Classify this cell by malaria status.
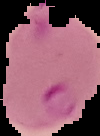

Parasitized.

Summary:
  - Image type: segmented cell region on a black background
  - Image size: 100×136 pixels
  - Preparation: thin blood smear